Classify this cell by malaria status.
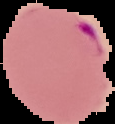

Parasitized.

preparation = thin blood smear
image type = segmented cell region with the area outside set to black
image size = 115×124 pixels